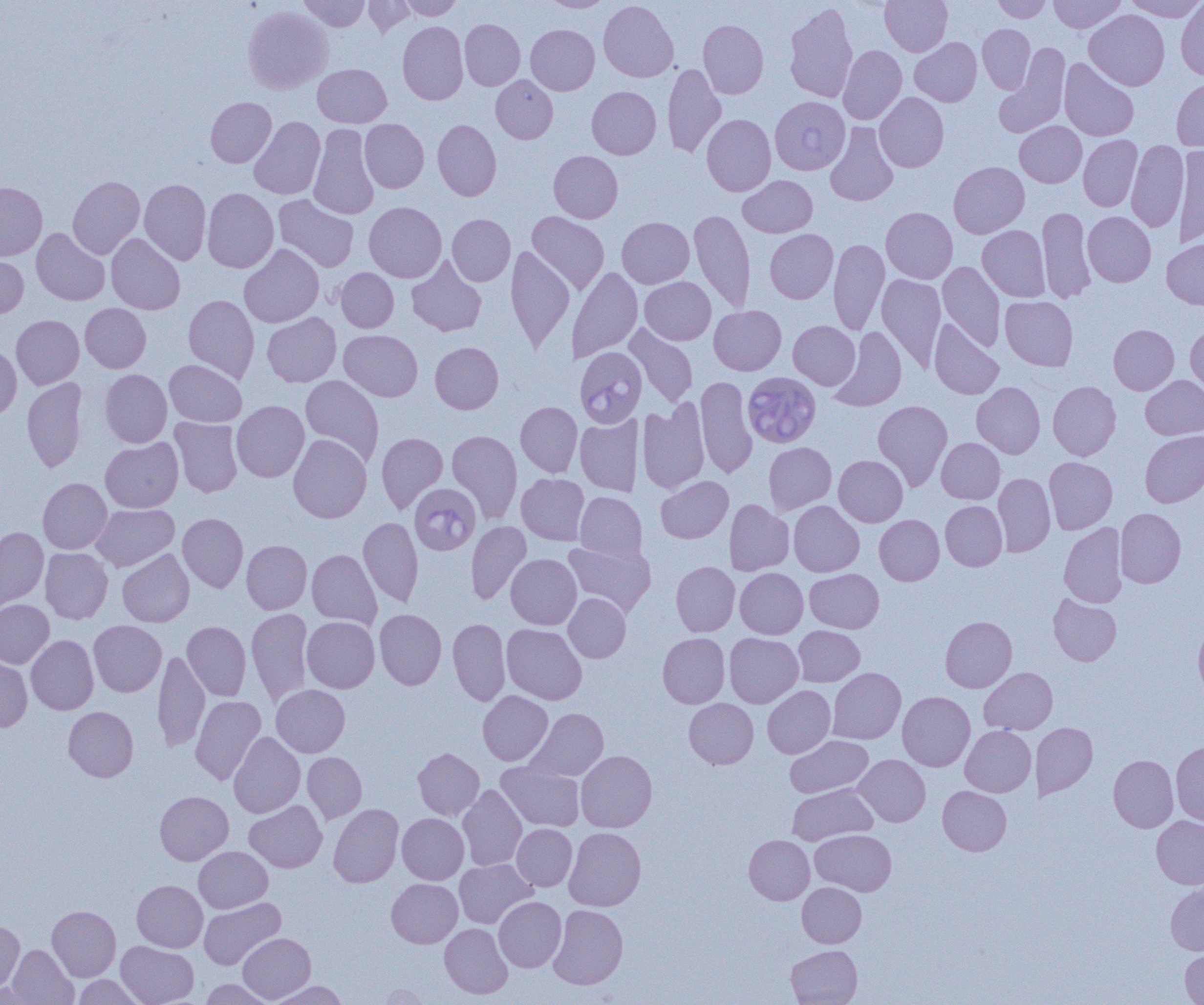
slide_level_diagnosis: Babesia divergens
magnification: 1000x
babesia_divergens_infected_red_blood_cell_locations: 'approximate bounding boxes as [x1, y1, x2, y2] in pixels: [770, 96, 850, 175], [576, 348, 645, 428], [746, 378, 824, 450], [410, 482, 481, 552]'
field_of_view: one of a larger specimen
modality: light microscopy
image_size: 1204×1005 pixels
preparation: thin blood film
uninfected_red_blood_cell_locations: 'approximate bounding boxes as [x1, y1, x2, y2] in pixels: [299, 0, 370, 31], [363, 0, 416, 36], [398, 0, 463, 20], [541, 0, 613, 12], [599, 0, 678, 82], [880, 0, 952, 56], [991, 0, 1052, 23], [1048, 0, 1125, 33], [1123, 0, 1204, 21], [1175, 1, 1204, 80], [784, 4, 858, 103], [243, 6, 333, 94], [1084, 10, 1170, 90], [460, 19, 525, 91], [698, 20, 768, 99], [398, 21, 468, 105], [526, 24, 600, 95], [977, 24, 1035, 94], [910, 37, 982, 106], [838, 45, 907, 125], [995, 46, 1070, 138], [1059, 58, 1139, 141], [663, 63, 726, 158], [313, 64, 392, 128], [491, 75, 558, 143], [1171, 77, 1204, 152], [587, 86, 661, 159], [875, 92, 949, 172], [206, 97, 276, 167], [702, 114, 776, 196], [249, 117, 325, 199], [359, 119, 429, 193], [433, 119, 501, 201], [1015, 121, 1086, 187], [308, 123, 379, 219], [825, 123, 899, 206], [1078, 135, 1143, 211], [1126, 140, 1189, 232], [1175, 144, 1204, 248], [549, 151, 623, 223], [948, 161, 1029, 238], [738, 175, 817, 238], [68, 176, 144, 258], [139, 179, 211, 264], [0, 182, 47, 261], [202, 188, 278, 273], [274, 195, 359, 272], [364, 202, 446, 283], [1037, 206, 1096, 303], [881, 207, 958, 283], [689, 209, 755, 312], [527, 211, 609, 294], [1083, 212, 1156, 287], [447, 214, 515, 286], [617, 217, 694, 288], [978, 225, 1050, 301], [31, 228, 110, 306], [765, 229, 838, 303], [106, 233, 185, 315], [828, 238, 889, 335], [1162, 238, 1204, 310], [239, 244, 324, 328], [506, 246, 574, 351], [0, 254, 29, 318], [407, 255, 487, 337], [938, 262, 1005, 351], [567, 267, 643, 362], [335, 268, 399, 332], [876, 273, 946, 371], [640, 277, 716, 345], [183, 294, 259, 383], [1000, 296, 1078, 371], [80, 304, 151, 372], [709, 305, 786, 375], [262, 312, 341, 387], [11, 315, 84, 389], [788, 320, 860, 390], [929, 320, 1004, 399], [624, 323, 699, 408], [1109, 324, 1179, 395], [1185, 324, 1204, 394], [830, 326, 907, 412], [339, 330, 422, 401], [430, 342, 503, 414], [0, 344, 21, 419], [164, 359, 246, 427], [100, 367, 245, 438], [100, 369, 172, 448], [300, 375, 384, 466], [695, 375, 758, 479], [1141, 375, 1204, 439], [22, 377, 87, 472], [1048, 381, 1121, 460], [972, 382, 1045, 458], [637, 399, 709, 495], [873, 400, 952, 490], [231, 401, 309, 482], [516, 401, 582, 477], [575, 414, 643, 496], [170, 417, 243, 497], [447, 430, 522, 523], [1140, 430, 1204, 507], [376, 432, 448, 514], [288, 433, 372, 523], [100, 438, 183, 512], [936, 438, 1005, 504], [764, 442, 836, 514], [833, 455, 908, 527], [1044, 457, 1117, 534], [516, 473, 590, 545], [993, 473, 1055, 556], [656, 476, 733, 543], [38, 478, 112, 554], [575, 491, 646, 565], [725, 499, 794, 576], [788, 500, 864, 577], [940, 501, 1007, 571], [91, 504, 179, 572], [1115, 508, 1186, 587], [177, 513, 248, 592], [874, 515, 944, 585], [358, 516, 423, 607], [466, 520, 531, 605], [1059, 522, 1127, 607], [0, 526, 48, 613], [241, 540, 312, 614], [563, 540, 655, 616], [40, 547, 113, 624], [117, 549, 194, 627], [307, 549, 382, 630], [506, 554, 581, 629], [671, 561, 739, 636], [735, 568, 808, 639], [805, 569, 884, 633], [564, 593, 631, 663], [1049, 594, 1121, 665], [0, 599, 54, 669], [246, 608, 313, 706], [374, 609, 446, 690], [302, 616, 379, 693], [940, 616, 1017, 692], [447, 618, 511, 706], [89, 620, 166, 697], [182, 621, 251, 701], [1193, 621, 1204, 701], [501, 623, 587, 704], [794, 625, 864, 686], [658, 633, 730, 708], [724, 633, 803, 708], [26, 635, 98, 715], [153, 650, 210, 752], [0, 655, 32, 732], [979, 667, 1057, 735], [828, 668, 906, 744], [271, 684, 350, 757], [763, 685, 835, 758], [478, 691, 553, 765], [898, 691, 975, 771], [190, 696, 266, 784], [684, 698, 758, 769], [63, 706, 138, 781], [526, 708, 608, 781], [1031, 722, 1098, 800], [960, 725, 1036, 797], [228, 731, 305, 818], [785, 735, 873, 798], [1171, 742, 1204, 826], [413, 747, 484, 820], [576, 750, 657, 832], [302, 752, 366, 824], [854, 754, 931, 826], [1109, 755, 1178, 832], [496, 762, 585, 831], [787, 784, 877, 845], [458, 785, 527, 871], [937, 786, 1011, 855], [155, 791, 233, 865], [244, 800, 327, 872], [329, 803, 403, 888], [397, 813, 468, 884], [1151, 816, 1204, 889], [512, 824, 577, 891], [564, 827, 646, 911], [811, 829, 896, 896], [744, 835, 814, 904], [194, 846, 273, 913], [454, 859, 536, 928], [387, 878, 462, 948], [132, 880, 207, 952], [797, 882, 866, 947], [1165, 884, 1204, 955], [494, 896, 566, 972], [199, 897, 285, 970], [548, 904, 628, 989], [47, 905, 121, 981], [0, 920, 25, 994], [439, 923, 513, 999], [238, 933, 316, 1003], [116, 941, 198, 1005], [7, 944, 78, 1005], [786, 945, 862, 1005], [1180, 947, 1204, 1005], [72, 975, 144, 1004], [201, 979, 273, 1005], [265, 980, 347, 1005], [376, 983, 431, 1004]'